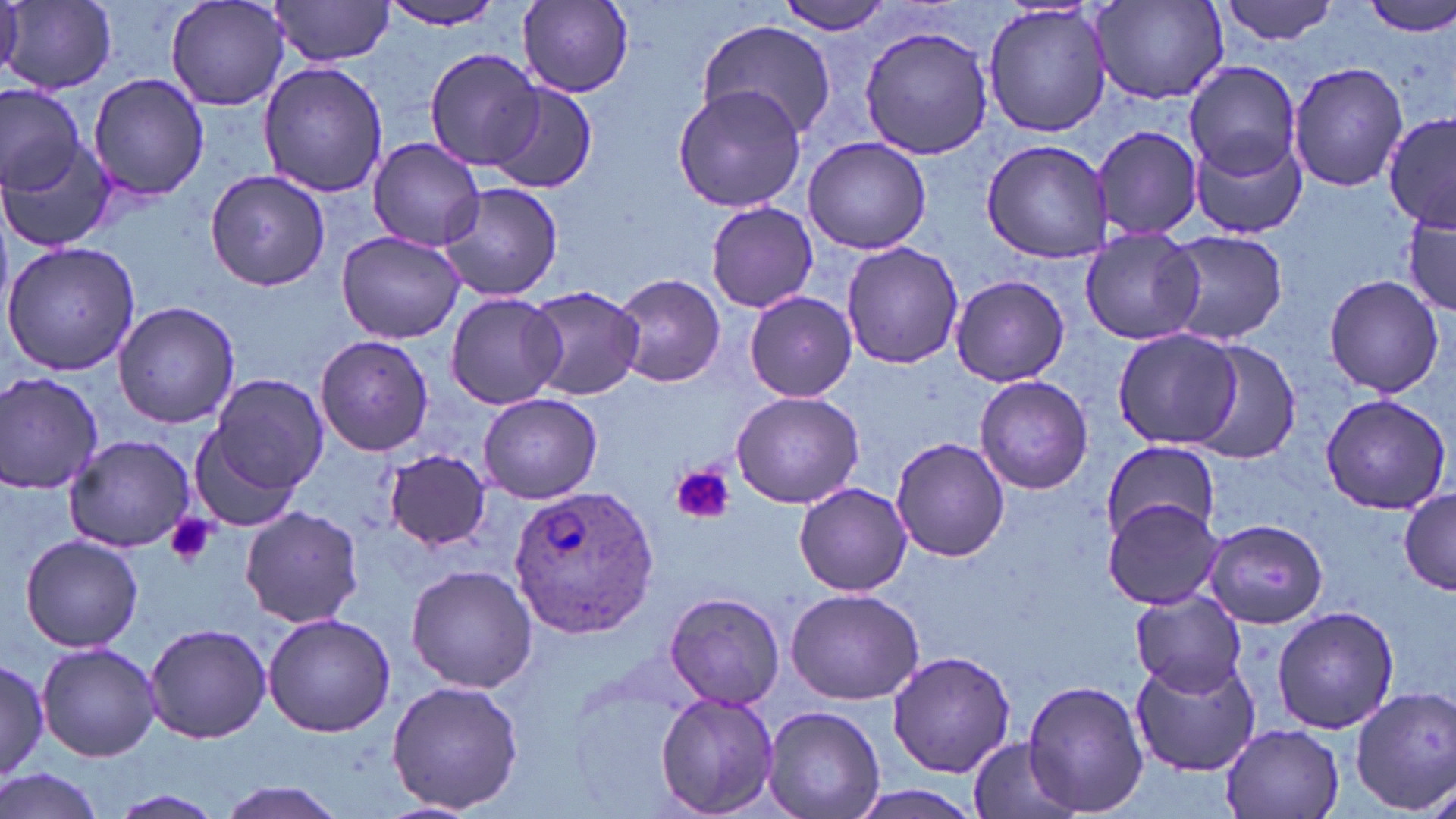

Summary:
  - Coordinate format: approximate bounding boxes as (x1, y1, x2, y2) in pixels
  - Uninfected red blood cell locations: (165, 0, 294, 112), (267, 0, 396, 66), (380, 0, 509, 30), (774, 0, 896, 35), (1217, 0, 1344, 46), (518, 1, 636, 97), (1089, 1, 1229, 107), (5, 2, 117, 92), (1362, 2, 1456, 37), (984, 3, 1110, 137), (698, 19, 836, 138), (858, 23, 995, 160), (425, 48, 545, 170), (258, 61, 386, 197), (1288, 61, 1409, 193), (1186, 63, 1304, 183), (88, 73, 211, 201), (489, 84, 596, 194), (671, 85, 809, 211), (0, 88, 83, 195), (1385, 112, 1456, 234), (1089, 124, 1204, 242), (1188, 130, 1308, 240), (802, 135, 932, 255), (368, 137, 484, 250), (2, 138, 119, 255), (980, 139, 1111, 264), (206, 171, 330, 291), (437, 180, 563, 303), (705, 200, 818, 314), (1403, 210, 1456, 319), (1081, 227, 1207, 346), (1158, 227, 1293, 347), (338, 231, 462, 344), (1, 241, 140, 377), (840, 241, 964, 370), (610, 272, 725, 388), (949, 274, 1069, 386), (1323, 276, 1445, 399), (522, 286, 645, 401), (445, 290, 564, 409), (743, 291, 859, 402), (112, 301, 240, 429), (1111, 325, 1246, 449), (315, 336, 435, 456), (1188, 340, 1302, 465), (0, 374, 104, 496), (211, 375, 328, 494), (973, 375, 1094, 495), (729, 390, 864, 509), (478, 392, 602, 502), (1320, 393, 1453, 514), (190, 423, 306, 535), (64, 433, 198, 552), (890, 437, 1011, 563), (1100, 441, 1223, 540), (384, 449, 493, 549), (794, 482, 912, 597), (1398, 489, 1454, 593), (1102, 498, 1225, 608), (239, 507, 366, 628), (1206, 519, 1330, 629), (19, 534, 145, 652), (407, 564, 539, 694), (785, 587, 923, 705), (663, 591, 786, 710), (1131, 591, 1246, 696), (1272, 607, 1398, 734), (262, 613, 396, 737), (145, 622, 270, 744), (37, 642, 160, 761), (886, 650, 1017, 778), (1130, 656, 1259, 776), (0, 658, 49, 783), (1022, 678, 1147, 815), (386, 680, 525, 814), (1350, 687, 1456, 812), (653, 690, 779, 818), (760, 704, 885, 819), (1219, 723, 1347, 818), (969, 737, 1083, 818), (0, 768, 108, 819), (211, 779, 353, 819), (846, 784, 989, 819), (107, 790, 228, 818), (374, 801, 484, 819)
  - Platelet locations: (672, 465, 734, 526), (165, 513, 218, 566)
  - Plasmodium ovale-infected red blood cell locations: (508, 483, 661, 637)
  - Slide-level diagnosis: Plasmodium ovale
  - Magnification: 1000x
  - Modality: light microscopy
  - Field of view: single
  - Stain: May-Grünwald-Giemsa
  - Preparation: thin blood film
  - Image size: 1456×819 pixels